Classify this cell by malaria status.
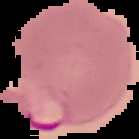
It is parasitized.

Summary:
  - Preparation: thin blood film
  - Image size: 139×139 pixels
  - Image type: cell region segmented out of the field of view; surrounding area masked to black